Identify the cell.
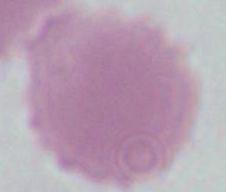
This is an erythrocyte.

Summary:
  - Magnification: 1000x
  - Modality: photomicrograph